Assess the morphology of the erythrocytes.
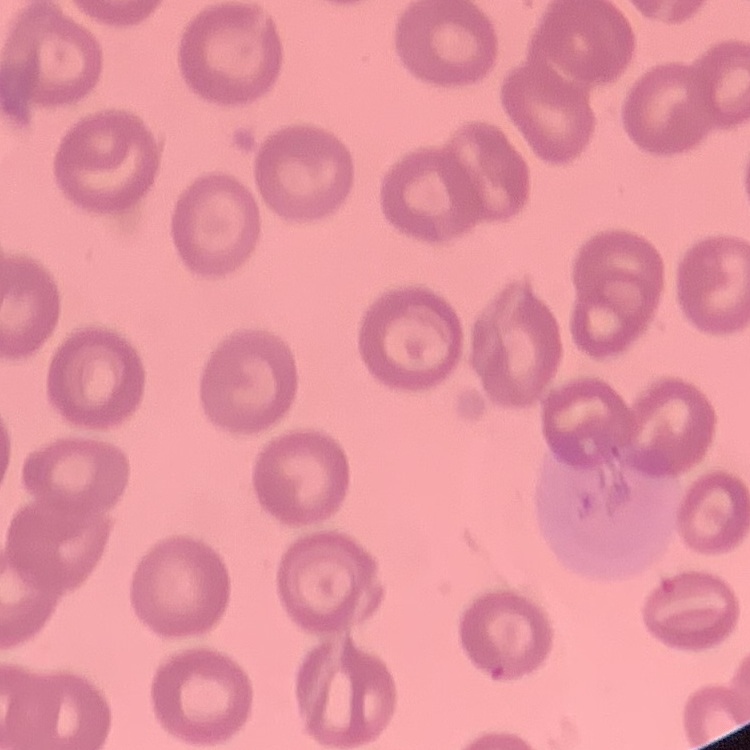

They show no rouleaux formation.

Field's or Giemsa stain. One tile cut from a larger photomicrograph. Thin blood smear.